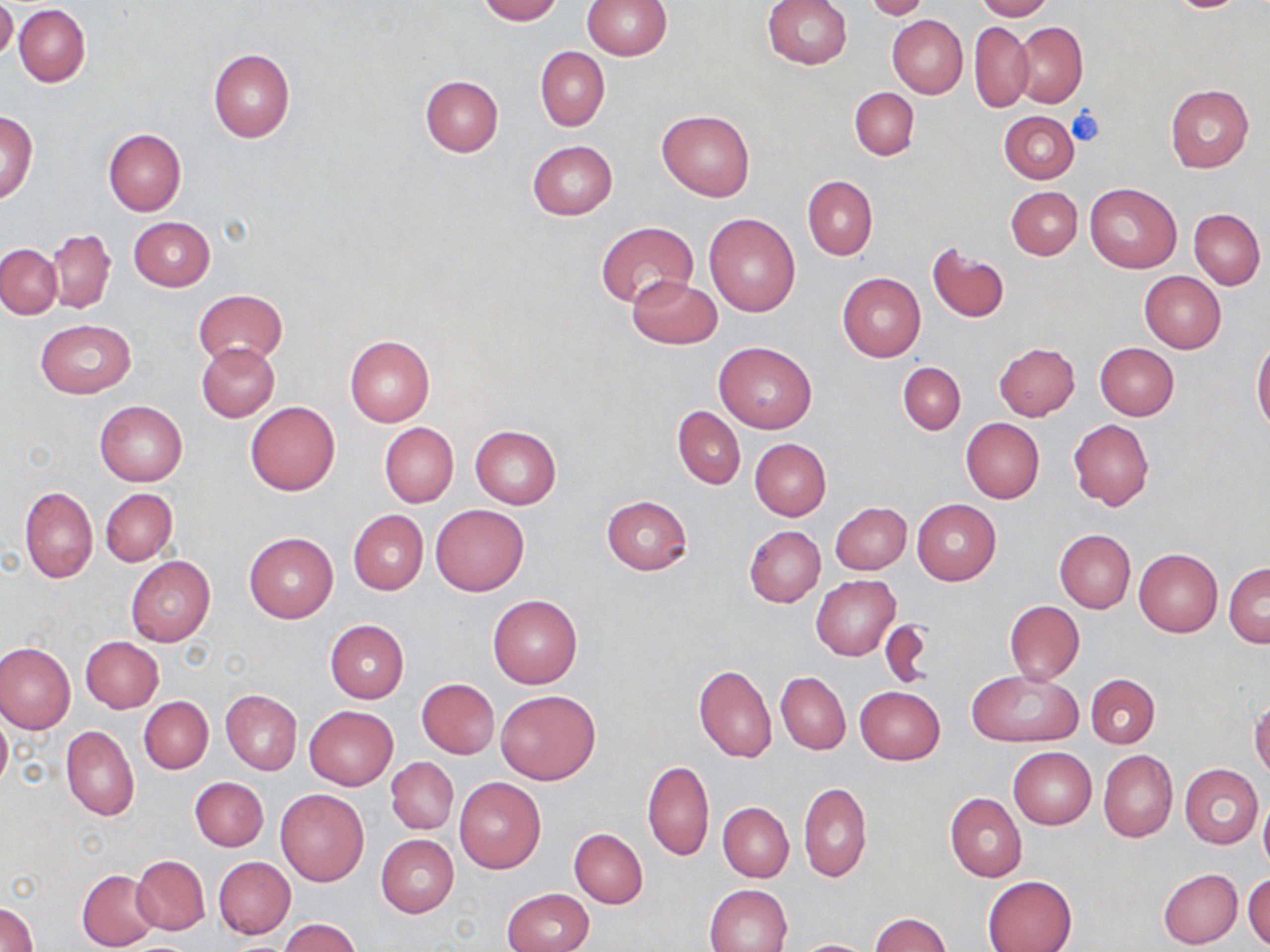
Approximate bounding boxes as (x1,y1)-(x2,y2) corner pairs in pixels. Platelet locations: (1067,106)-(1104,146). Uninfected red blood cell locations: (0,0)-(17,62), (476,0)-(561,23), (582,0)-(671,59), (760,0)-(852,70), (976,0)-(1052,20), (864,1)-(929,20), (14,4)-(90,86), (887,15)-(968,98), (970,22)-(1033,113), (1013,22)-(1087,107), (535,46)-(609,130), (208,49)-(295,142), (420,76)-(503,156), (1165,85)-(1252,173), (850,88)-(918,159), (1,110)-(37,203), (656,110)-(755,200), (999,111)-(1078,183), (104,129)-(186,215), (528,141)-(617,219), (802,175)-(877,259), (1085,181)-(1181,273), (1006,187)-(1082,260), (1189,209)-(1266,288), (704,212)-(801,317), (129,216)-(215,290), (596,221)-(697,310), (46,230)-(114,313), (927,243)-(1010,323), (0,244)-(62,318), (1139,271)-(1226,353), (837,273)-(925,362), (627,275)-(721,349), (195,289)-(286,367), (35,319)-(136,398), (344,335)-(435,427), (714,340)-(817,434), (197,341)-(279,421), (1252,341)-(1270,433), (994,342)-(1080,420), (1095,343)-(1179,421), (898,362)-(965,434), (94,401)-(187,485), (244,401)-(340,495), (673,406)-(745,489), (961,418)-(1045,503), (1068,418)-(1154,511), (379,422)-(458,507), (469,424)-(562,508), (750,439)-(830,520), (19,486)-(98,583), (100,488)-(177,567), (600,495)-(692,575), (911,499)-(1000,586), (830,501)-(911,574), (431,504)-(529,596), (348,509)-(428,595), (744,525)-(825,607), (1055,530)-(1135,612), (243,532)-(338,623), (1133,548)-(1222,637), (126,557)-(215,646), (1224,562)-(1269,647), (812,576)-(899,660), (488,595)-(582,688), (1004,600)-(1084,685), (876,616)-(935,690), (325,620)-(408,703), (81,636)-(164,712), (0,642)-(75,733), (693,664)-(776,763), (967,669)-(1082,748), (777,672)-(851,755), (1086,673)-(1159,748), (417,678)-(499,759), (854,685)-(944,764), (495,688)-(600,785), (221,690)-(301,774), (138,696)-(213,773), (1250,698)-(1270,778), (305,706)-(397,789), (0,709)-(11,792), (61,725)-(139,821), (1008,747)-(1096,829), (1099,750)-(1177,842), (386,756)-(458,834), (642,761)-(714,861), (1180,764)-(1263,848), (190,777)-(267,851), (454,777)-(546,874), (798,782)-(871,882), (275,789)-(369,886), (945,792)-(1026,881), (1259,799)-(1270,875), (719,803)-(794,882), (569,828)-(648,908), (376,834)-(458,917), (132,855)-(210,934), (213,857)-(295,939), (76,869)-(161,950), (1158,869)-(1242,948), (1244,872)-(1270,949), (982,875)-(1076,952), (705,884)-(792,952), (502,888)-(595,952), (1,901)-(37,952), (868,913)-(952,951), (278,918)-(361,952), (798,940)-(871,952). Slide-level diagnosis: negative for blood parasites. Optical microscopy. 1000x magnification. Single field of view. Image is 1270×952 pixels. Thin blood smear. May-Grünwald-Giemsa-stained preparation.